Name the parasite shown.
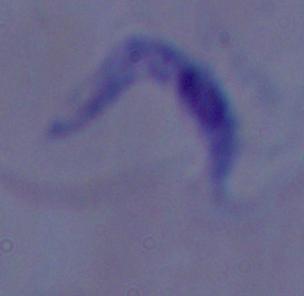
This is a trypanosome.

magnification: 1000x
modality: micrograph